Locate every Plasmodium malariae-infected red blood cell.
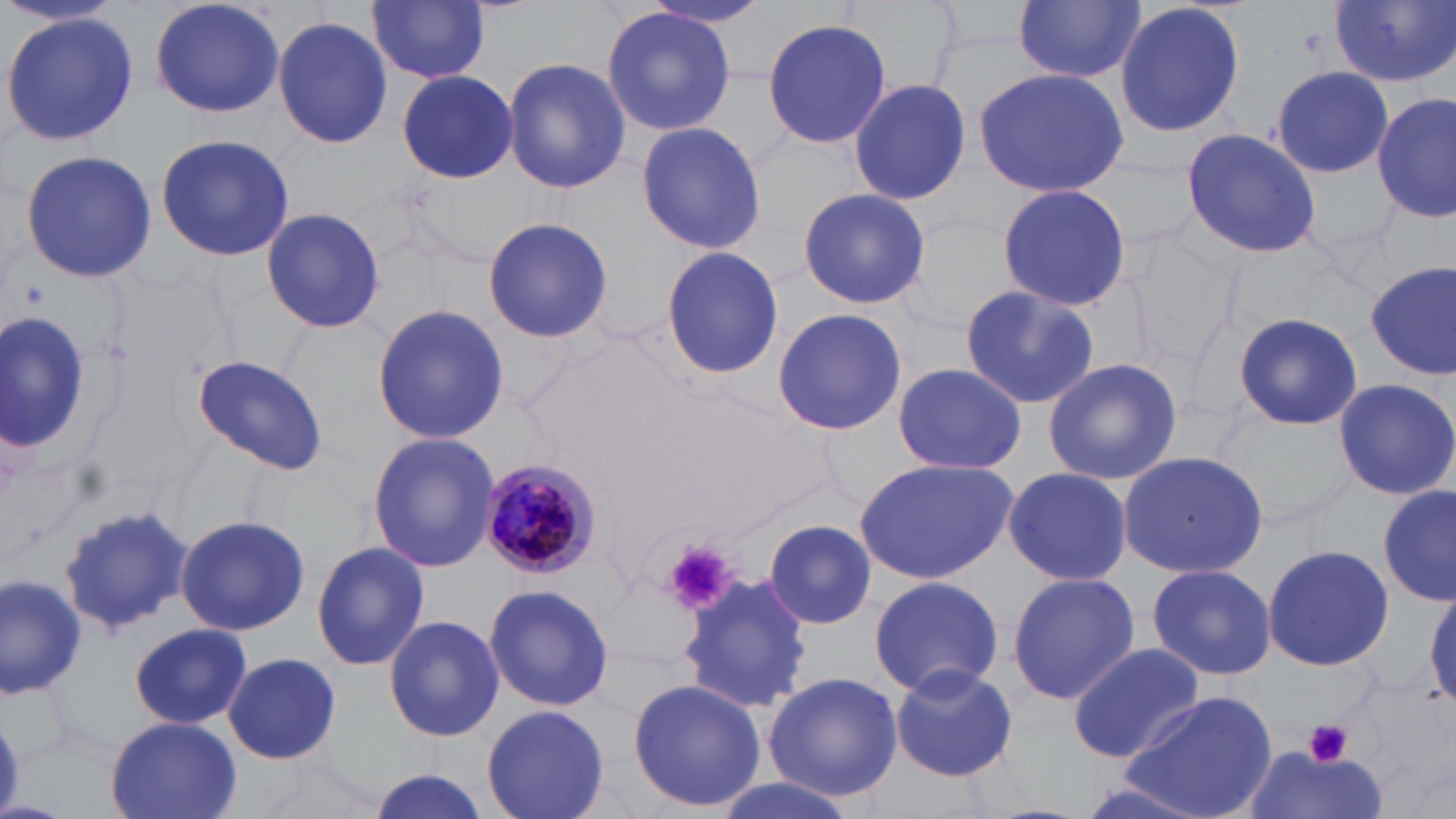

Approximate bounding boxes as (x1,y1)-(x2,y2) corner pairs in pixels.
Plasmodium malariae-infected red blood cells: (476,455)-(597,580).

Platelet locations: (663,540)-(734,614), (1304,718)-(1353,767). Uninfected red blood cell locations: (150,0)-(284,118), (640,0)-(773,32), (1328,0)-(1456,88), (369,1)-(490,84), (1015,1)-(1143,83), (1114,1)-(1245,140), (600,7)-(735,137), (1,14)-(138,145), (273,15)-(392,151), (762,16)-(891,150), (503,58)-(630,195), (1271,65)-(1393,178), (973,66)-(1129,198), (397,69)-(519,184), (848,77)-(973,207), (1373,93)-(1456,224), (634,122)-(768,253), (1178,126)-(1321,259), (155,134)-(295,261), (20,150)-(156,283), (994,184)-(1134,311), (797,188)-(931,311), (261,206)-(385,333), (482,215)-(614,343), (1124,229)-(1243,371), (658,244)-(786,381), (1365,261)-(1454,381), (958,284)-(1100,411), (372,304)-(510,444), (771,309)-(909,436), (0,312)-(90,454), (1232,312)-(1363,430), (190,353)-(330,476), (1042,356)-(1183,485), (891,362)-(1027,476), (1333,376)-(1456,500), (368,430)-(500,573), (1116,450)-(1270,578), (854,457)-(1018,583), (1001,467)-(1132,587), (1380,485)-(1454,606), (57,505)-(193,636), (176,514)-(309,637), (763,519)-(876,631), (311,539)-(430,672), (1262,542)-(1392,674), (1146,562)-(1277,680), (1007,571)-(1139,705), (0,573)-(88,698), (680,573)-(810,715), (866,574)-(1006,695), (483,583)-(615,712), (384,613)-(505,742), (129,623)-(252,729), (1066,644)-(1205,762), (224,653)-(343,766), (889,664)-(1018,782), (762,671)-(902,799), (629,678)-(767,812), (1122,691)-(1279,819), (482,704)-(611,819), (105,717)-(242,819), (1242,746)-(1386,819), (366,768)-(493,819), (706,775)-(862,819). Slide-level diagnosis: Plasmodium malariae. Image is 1456×819 pixels. May-Grünwald-Giemsa stain. Single field of view. Thin blood smear. Optical microscopy. Captured at 1000x magnification.